Outline each blood parasite and name the species.
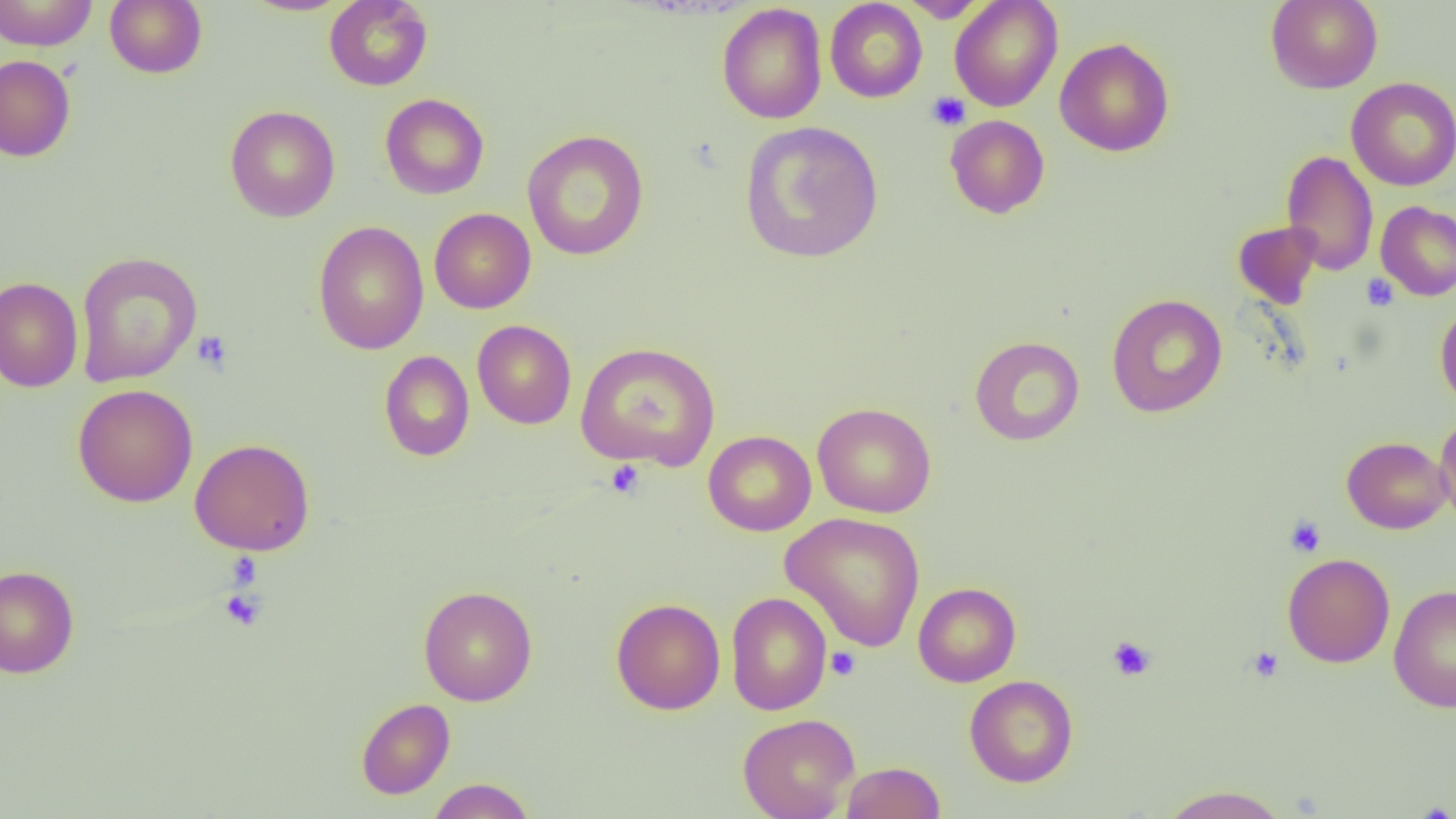
No blood parasites seen.

Summary:
  - Coordinate format: approximate bounding boxes as named x1/y1/x2/y2 corners in pixels
  - Platelet locations: (x1=926, y1=91, x2=970, y2=130), (x1=1361, y1=273, x2=1399, y2=311), (x1=191, y1=330, x2=233, y2=373), (x1=605, y1=460, x2=645, y2=500), (x1=1285, y1=516, x2=1326, y2=557), (x1=224, y1=552, x2=263, y2=589), (x1=219, y1=588, x2=268, y2=632), (x1=1106, y1=635, x2=1156, y2=681), (x1=1246, y1=646, x2=1284, y2=683), (x1=826, y1=647, x2=861, y2=680)
  - Uninfected red blood cell locations: (x1=0, y1=0, x2=97, y2=51), (x1=105, y1=0, x2=207, y2=78), (x1=241, y1=0, x2=352, y2=16), (x1=324, y1=0, x2=433, y2=91), (x1=900, y1=0, x2=988, y2=22), (x1=949, y1=0, x2=1063, y2=111), (x1=1266, y1=0, x2=1383, y2=93), (x1=824, y1=1, x2=927, y2=102), (x1=717, y1=3, x2=827, y2=124), (x1=1055, y1=37, x2=1174, y2=157), (x1=0, y1=55, x2=76, y2=162), (x1=1346, y1=77, x2=1456, y2=191), (x1=379, y1=93, x2=489, y2=199), (x1=225, y1=105, x2=340, y2=223), (x1=945, y1=114, x2=1050, y2=219), (x1=740, y1=121, x2=883, y2=263), (x1=522, y1=129, x2=649, y2=260), (x1=1281, y1=149, x2=1378, y2=275), (x1=1376, y1=201, x2=1456, y2=300), (x1=429, y1=208, x2=536, y2=313), (x1=1232, y1=220, x2=1323, y2=309), (x1=313, y1=221, x2=429, y2=355), (x1=75, y1=251, x2=202, y2=387), (x1=0, y1=277, x2=84, y2=392), (x1=1105, y1=294, x2=1228, y2=417), (x1=1435, y1=302, x2=1456, y2=412), (x1=472, y1=320, x2=576, y2=429), (x1=969, y1=336, x2=1085, y2=446), (x1=575, y1=342, x2=721, y2=471), (x1=379, y1=350, x2=474, y2=461), (x1=72, y1=384, x2=198, y2=507), (x1=812, y1=402, x2=937, y2=518), (x1=1434, y1=412, x2=1456, y2=531), (x1=703, y1=430, x2=816, y2=536), (x1=1341, y1=437, x2=1453, y2=534), (x1=189, y1=438, x2=315, y2=555), (x1=780, y1=512, x2=926, y2=652), (x1=1282, y1=553, x2=1395, y2=667), (x1=0, y1=564, x2=79, y2=678), (x1=913, y1=582, x2=1021, y2=687), (x1=1389, y1=584, x2=1456, y2=713), (x1=418, y1=585, x2=538, y2=706), (x1=726, y1=592, x2=831, y2=715), (x1=611, y1=597, x2=725, y2=715), (x1=964, y1=675, x2=1078, y2=787), (x1=356, y1=698, x2=455, y2=799), (x1=738, y1=713, x2=859, y2=819), (x1=841, y1=761, x2=946, y2=819), (x1=427, y1=778, x2=536, y2=819), (x1=1157, y1=784, x2=1292, y2=819)
  - Slide-level diagnosis: negative for blood parasites
  - Preparation: thin blood film
  - Image size: 1456×819 pixels
  - Magnification: 1000x
  - Modality: optical microscopy
  - Field of view: one of a larger specimen